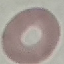
malaria_status: uninfected
stain: Giemsa
capture: smartphone camera at the microscope eyepiece
preparation: thin smear
image_type: automatically extracted cell patch, resized to 64 × 64 pixels